Classify this cell by malaria status.
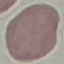

Uninfected.

{
  "capture": "smartphone camera at the microscope eyepiece",
  "preparation": "thin smear",
  "image_type": "automatically extracted cell patch, resized to 64 × 64 pixels",
  "stain": "Giemsa"
}